Locate and identify every blood parasite.
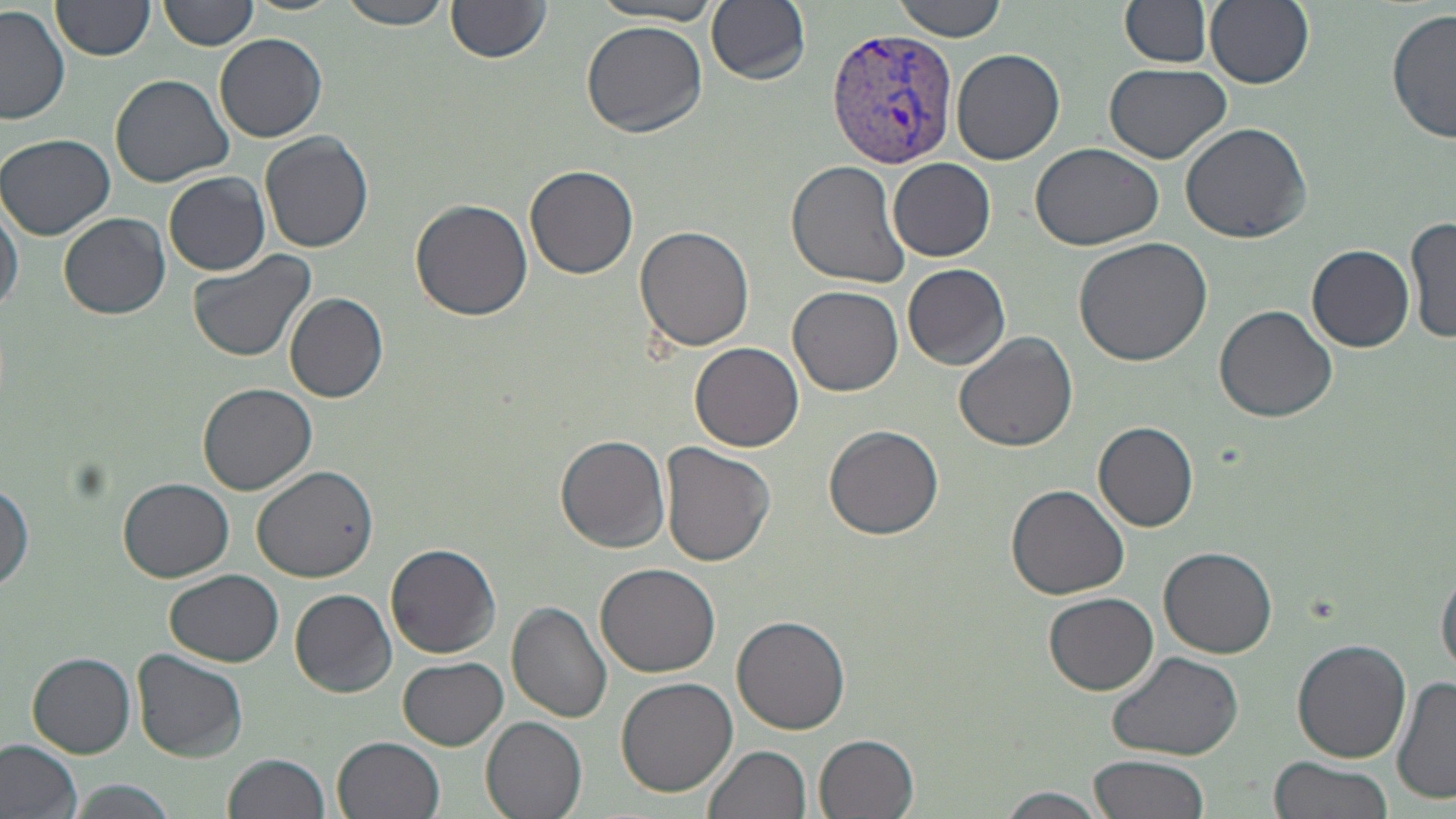
Approximate bounding boxes as (x1, y1, x2, y2) in pixels.
Plasmodium vivax-infected red blood cells: (825, 29, 957, 169).
No Plasmodium falciparum, Plasmodium ovale, Plasmodium malariae, Babesia divergens, or Trypanosoma brucei observed.

Summary:
  - Uninfected red blood cell locations: (336, 0, 454, 29), (893, 0, 1009, 42), (1205, 0, 1314, 89), (159, 1, 259, 51), (1123, 1, 1212, 66), (50, 2, 154, 62), (446, 2, 552, 65), (706, 2, 810, 85), (595, 3, 721, 25), (0, 5, 70, 124), (1388, 8, 1455, 145), (581, 21, 707, 137), (214, 31, 327, 142), (951, 47, 1065, 166), (1103, 61, 1232, 163), (112, 74, 232, 186), (1179, 121, 1312, 243), (1, 133, 118, 240), (261, 133, 374, 255), (1029, 142, 1166, 252), (785, 157, 913, 288), (889, 158, 994, 261), (525, 164, 638, 279), (164, 170, 270, 275), (0, 194, 22, 321), (410, 198, 533, 322), (60, 213, 171, 320), (1405, 217, 1456, 343), (634, 225, 756, 352), (1073, 237, 1212, 365), (1307, 244, 1414, 351), (186, 250, 316, 362), (902, 263, 1012, 369), (788, 286, 904, 397), (283, 292, 387, 402), (1213, 305, 1339, 423), (953, 331, 1078, 451), (691, 342, 805, 453), (198, 384, 317, 497), (1094, 421, 1200, 532), (824, 425, 944, 540), (556, 435, 671, 552), (662, 444, 776, 570), (253, 466, 378, 583), (0, 476, 32, 596), (119, 478, 234, 581), (1006, 484, 1131, 601), (385, 544, 500, 659), (1158, 545, 1279, 658), (1437, 559, 1456, 678), (594, 563, 722, 678), (166, 569, 283, 667), (289, 587, 396, 697), (1045, 593, 1159, 695), (507, 601, 613, 722), (732, 613, 851, 735), (1291, 637, 1412, 764), (1105, 649, 1244, 762), (131, 650, 249, 762), (27, 653, 136, 756), (399, 656, 507, 749), (1393, 674, 1456, 807), (616, 676, 738, 796), (481, 716, 589, 819), (815, 733, 921, 819), (333, 735, 446, 819), (0, 739, 83, 817), (705, 744, 813, 819), (226, 753, 332, 819), (1091, 753, 1211, 819), (1267, 757, 1392, 819), (66, 779, 179, 819), (991, 787, 1113, 819)
  - Slide-level diagnosis: Plasmodium vivax
  - Magnification: 1000x
  - Image size: 1456×819 pixels
  - Preparation: thin blood film
  - Field of view: single
  - Modality: light microscopy
  - Stain: May-Grünwald-Giemsa